Name the blood parasite species.
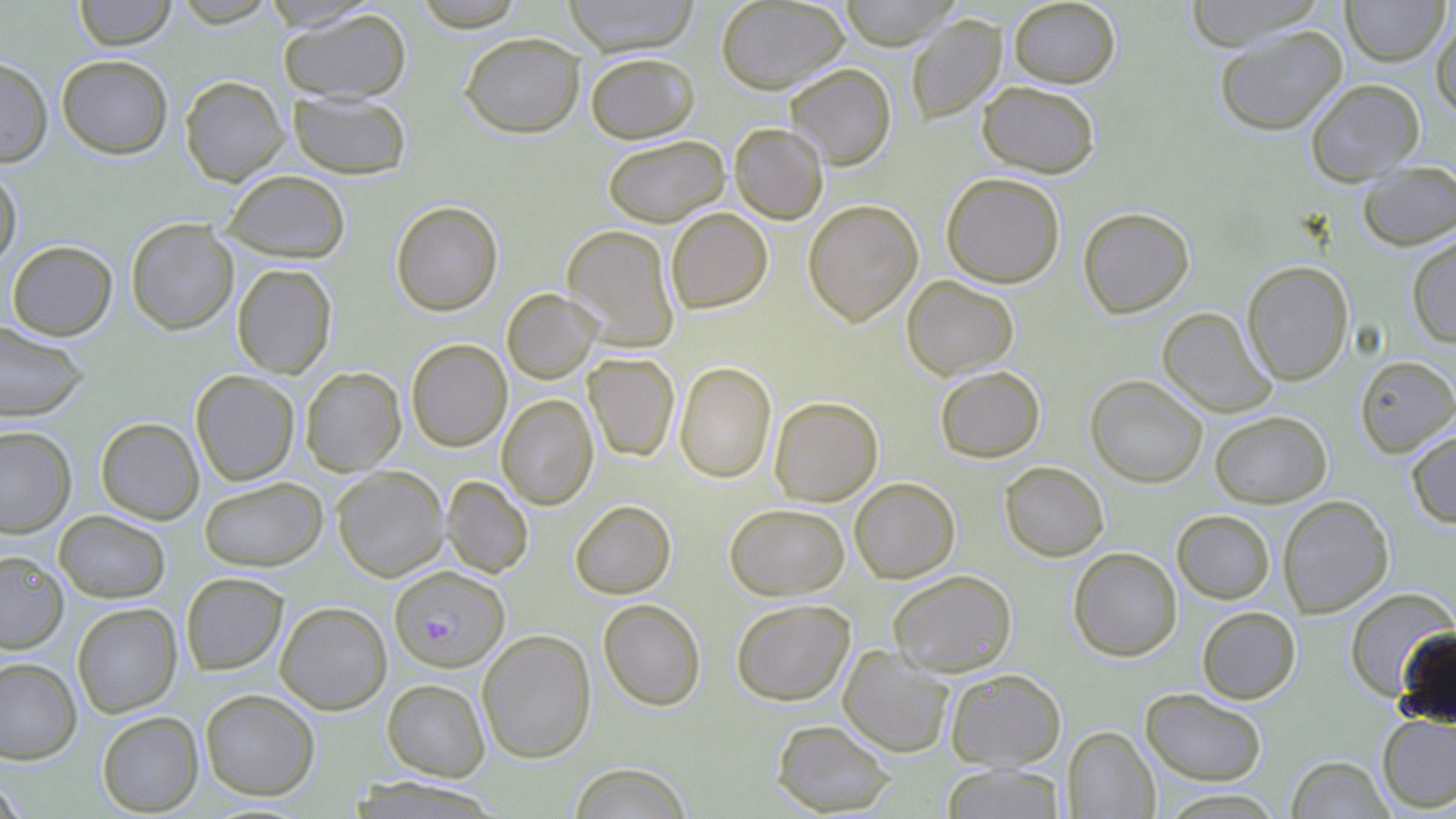
Plasmodium falciparum.

{
  "modality": "light microscopy",
  "magnification": "1000x",
  "stain": "May-Grünwald-Giemsa",
  "preparation": "thin blood film",
  "field_of_view": "one of a larger specimen",
  "plasmodium_falciparum_infected_red_blood_cell_locations": "approximate bounding boxes as named x1/y1/x2/y2 corners in pixels: (x1=391, y1=564, x2=511, y2=670)",
  "uninfected_red_blood_cell_locations": "approximate bounding boxes as named x1/y1/x2/y2 corners in pixels: (x1=73, y1=0, x2=177, y2=50), (x1=169, y1=0, x2=280, y2=27), (x1=411, y1=0, x2=528, y2=31), (x1=562, y1=0, x2=701, y2=56), (x1=716, y1=0, x2=849, y2=94), (x1=838, y1=0, x2=960, y2=50), (x1=1008, y1=0, x2=1120, y2=88), (x1=1182, y1=0, x2=1326, y2=50), (x1=1341, y1=0, x2=1449, y2=66), (x1=278, y1=7, x2=411, y2=103), (x1=906, y1=14, x2=1006, y2=124), (x1=1431, y1=18, x2=1456, y2=121), (x1=1214, y1=24, x2=1348, y2=136), (x1=459, y1=32, x2=585, y2=138), (x1=585, y1=52, x2=700, y2=143), (x1=57, y1=54, x2=173, y2=159), (x1=0, y1=57, x2=52, y2=167), (x1=785, y1=63, x2=897, y2=170), (x1=180, y1=75, x2=289, y2=186), (x1=1305, y1=78, x2=1424, y2=185), (x1=976, y1=81, x2=1100, y2=178), (x1=288, y1=91, x2=412, y2=180), (x1=729, y1=123, x2=828, y2=224), (x1=602, y1=135, x2=730, y2=227), (x1=1357, y1=160, x2=1456, y2=251), (x1=0, y1=165, x2=22, y2=270), (x1=221, y1=169, x2=351, y2=263), (x1=941, y1=172, x2=1065, y2=288), (x1=803, y1=199, x2=923, y2=326), (x1=391, y1=200, x2=503, y2=316), (x1=1078, y1=206, x2=1194, y2=318), (x1=666, y1=207, x2=772, y2=313), (x1=126, y1=218, x2=239, y2=335), (x1=562, y1=224, x2=680, y2=352), (x1=1406, y1=231, x2=1456, y2=348), (x1=7, y1=240, x2=117, y2=340), (x1=1242, y1=260, x2=1353, y2=385), (x1=232, y1=263, x2=337, y2=378), (x1=902, y1=274, x2=1019, y2=380), (x1=502, y1=288, x2=601, y2=383), (x1=1157, y1=307, x2=1276, y2=418), (x1=0, y1=321, x2=88, y2=422), (x1=406, y1=339, x2=512, y2=452), (x1=583, y1=352, x2=680, y2=461), (x1=1355, y1=355, x2=1456, y2=458), (x1=675, y1=361, x2=776, y2=483), (x1=300, y1=366, x2=406, y2=476), (x1=934, y1=366, x2=1045, y2=462), (x1=190, y1=370, x2=300, y2=485), (x1=1086, y1=375, x2=1208, y2=488), (x1=497, y1=394, x2=598, y2=510), (x1=769, y1=396, x2=883, y2=506), (x1=1210, y1=410, x2=1331, y2=507), (x1=96, y1=417, x2=204, y2=524), (x1=0, y1=425, x2=76, y2=537), (x1=1406, y1=429, x2=1456, y2=528), (x1=999, y1=461, x2=1109, y2=561), (x1=332, y1=465, x2=449, y2=581), (x1=441, y1=475, x2=534, y2=579), (x1=199, y1=477, x2=327, y2=571), (x1=850, y1=477, x2=960, y2=583), (x1=1278, y1=495, x2=1394, y2=618), (x1=570, y1=500, x2=676, y2=599), (x1=724, y1=503, x2=849, y2=600), (x1=54, y1=510, x2=171, y2=603), (x1=1172, y1=510, x2=1275, y2=603), (x1=1068, y1=547, x2=1182, y2=661), (x1=0, y1=550, x2=69, y2=653), (x1=888, y1=569, x2=1017, y2=677), (x1=180, y1=572, x2=288, y2=675), (x1=1344, y1=588, x2=1455, y2=701), (x1=598, y1=599, x2=706, y2=711), (x1=731, y1=599, x2=855, y2=705), (x1=275, y1=601, x2=392, y2=714), (x1=72, y1=603, x2=182, y2=717), (x1=1197, y1=606, x2=1301, y2=704), (x1=477, y1=628, x2=596, y2=763), (x1=838, y1=646, x2=955, y2=757), (x1=0, y1=657, x2=82, y2=764), (x1=945, y1=668, x2=1066, y2=770), (x1=382, y1=678, x2=490, y2=781), (x1=1140, y1=687, x2=1267, y2=787), (x1=200, y1=688, x2=320, y2=800), (x1=96, y1=711, x2=204, y2=816), (x1=1376, y1=713, x2=1456, y2=813), (x1=771, y1=719, x2=895, y2=816), (x1=1062, y1=726, x2=1159, y2=818), (x1=1286, y1=755, x2=1393, y2=818), (x1=569, y1=763, x2=692, y2=819), (x1=940, y1=763, x2=1066, y2=818), (x1=0, y1=776, x2=27, y2=818), (x1=347, y1=776, x2=505, y2=818), (x1=1154, y1=788, x2=1287, y2=818)",
  "image_size": "1456×819 pixels"
}